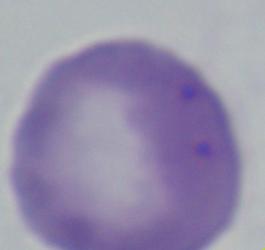
Summary:
  - Magnification: 1000x
  - Identification: Babesia
  - Modality: photomicrograph